Comment on the morphology of the erythrocytes.
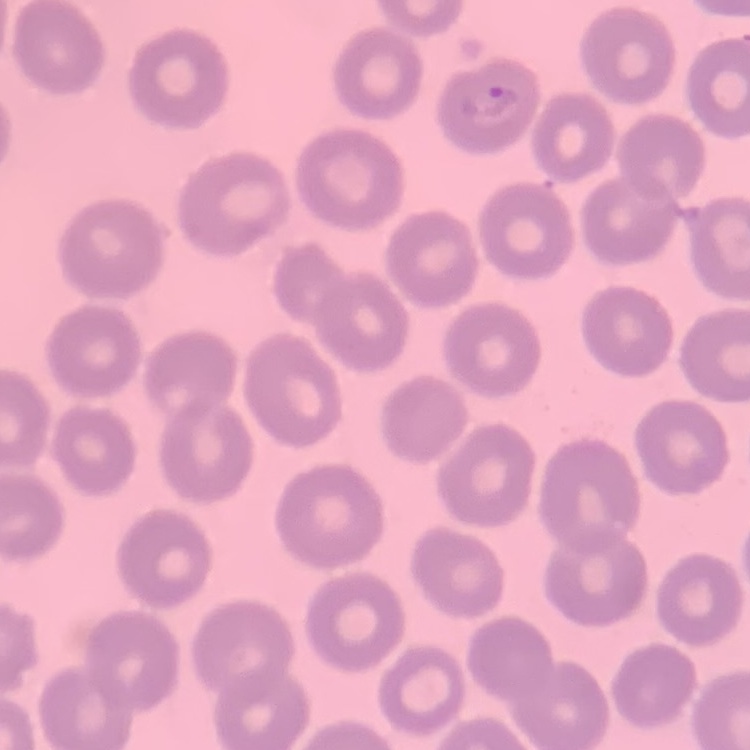

They show no rouleaux formation.

stain = Field's or Giemsa
preparation = thin blood smear
image type = square crop of a larger photomicrograph